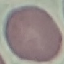

Malaria status: uninfected. Thin smear of blood. Acquired by smartphone through the microscope eyepiece. Giemsa-stained preparation. Automatically extracted cell patch, resized to 64 × 64 pixels.